Assess this cell for malaria.
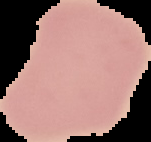

Uninfected.

{
  "image_type": "segmented cell region on a black background",
  "image_size": "151×142 pixels",
  "preparation": "thin blood film"
}